Give the position of every malaria parasite.
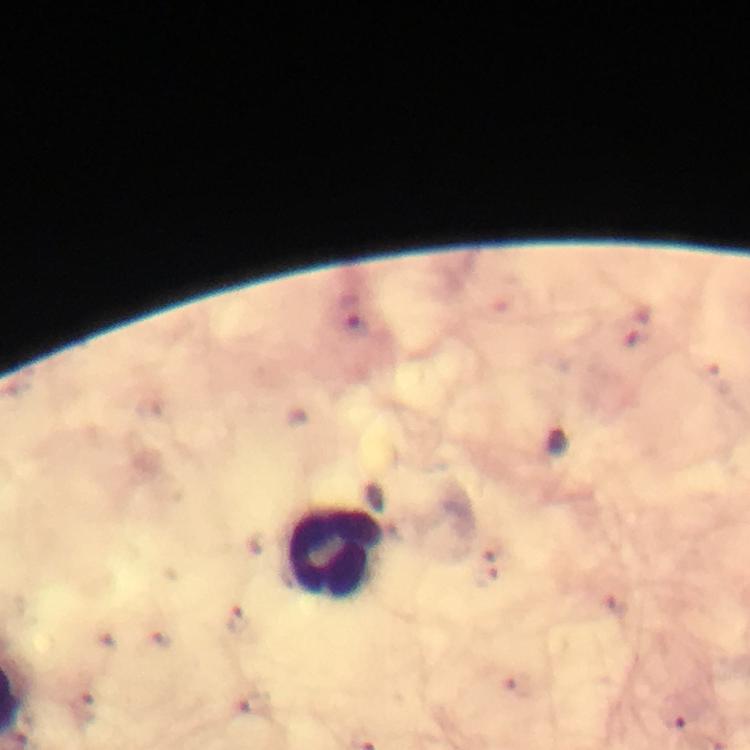

Approximate centers as {x, y} in pixels.
Malaria parasites: {355, 324}, {559, 443}, {484, 572}, {237, 619}, {253, 704}, {672, 717}.

{
  "leukocyte_locations": "approximate centers as {x, y} in pixels: {336, 553}",
  "immersion_oil": "used",
  "context": "from a malaria diagnostic workup",
  "cropped_from": "a single field of view",
  "stain": "Giemsa",
  "capture": "smartphone photograph through a microscope",
  "image_size": "750×750 pixels",
  "preparation": "thick blood smear",
  "magnification": "100x"
}